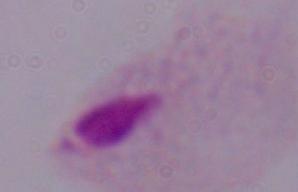 Micrograph. A trichomonad is shown. 1000x magnification.